Classify this cell by malaria status.
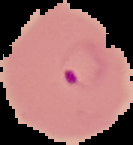
It is parasitized.

image_type: segmented cell region on a black background
image_size: 133×145 pixels
preparation: thin blood film